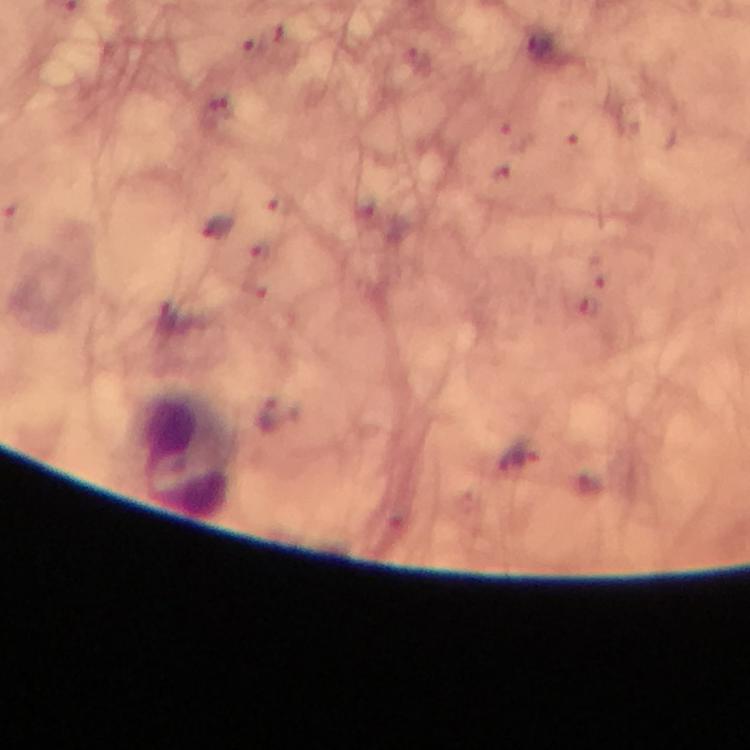

Approximate centers as (x, y) in pixels.
Summary:
  - Leukocyte locations: (185, 454)
  - Plasmodium parasite locations: (537, 44), (217, 228), (518, 455)
  - Stain: Giemsa
  - Cropped from: one field of view
  - Image size: 750×750 pixels
  - Preparation: thick blood film
  - Magnification: 100x
  - Context: from a diagnostic examination for malaria
  - Capture: smartphone camera through the microscope
  - Immersion oil: applied